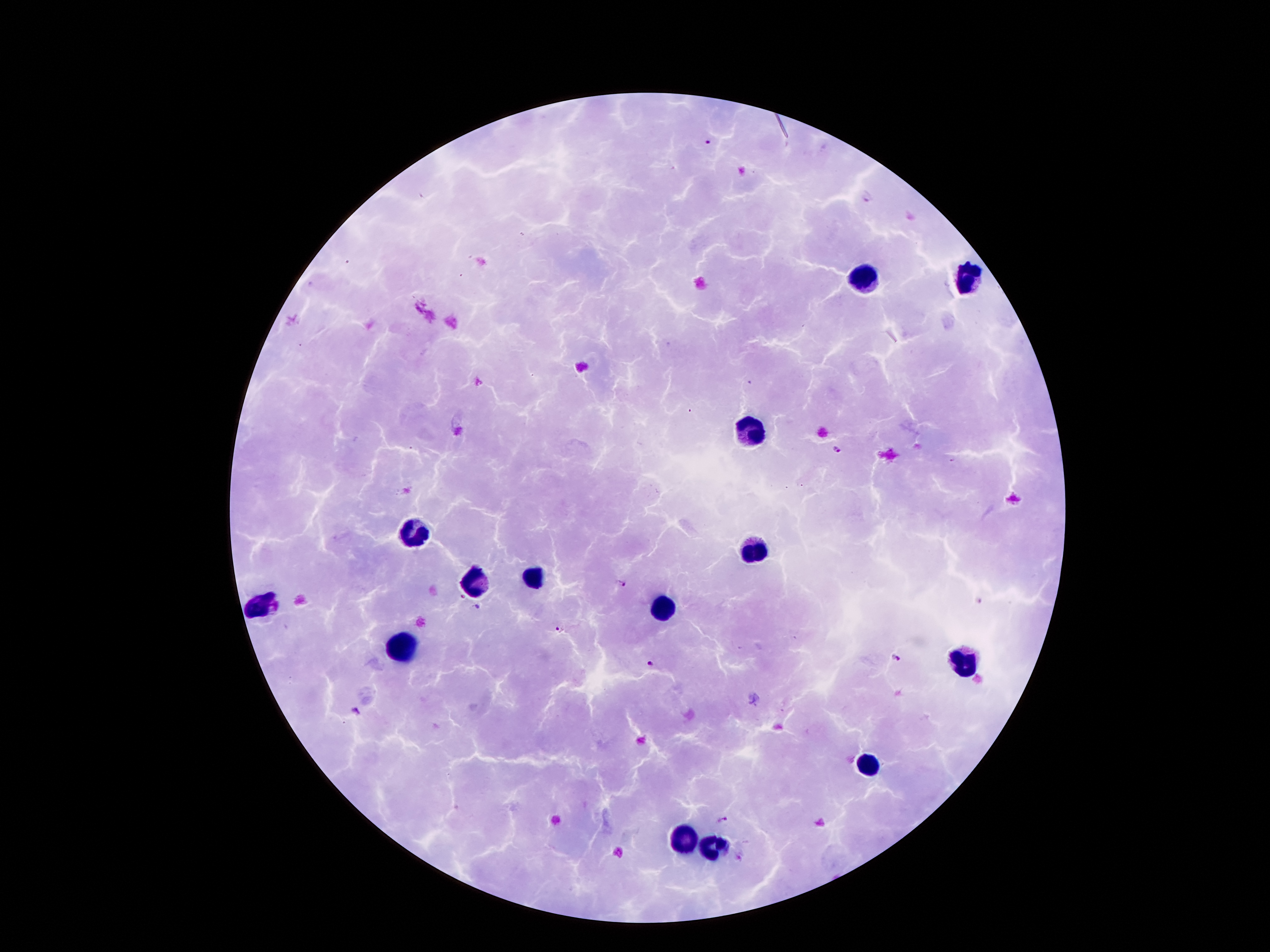
coordinate format = approximate centers as {x, y} in pixels
Plasmodium parasite locations = {709, 144}, {868, 195}, {838, 449}, {621, 582}, {978, 601}, {558, 630}, {895, 658}, {651, 663}, {355, 712}, {721, 819}
leukocyte locations = {864, 275}, {970, 275}, {751, 429}, {408, 532}, {753, 549}, {532, 575}, {472, 583}, {256, 604}, {667, 611}, {403, 643}, {962, 664}, {866, 765}, {684, 837}, {710, 844}
field of view = one from this slide
capture = smartphone camera through the microscope eyepiece
preparation = thick peripheral-blood smear
stain = Giemsa
image size = 1270×952 pixels
magnification = 100x
patient malaria status = positive for Plasmodium falciparum